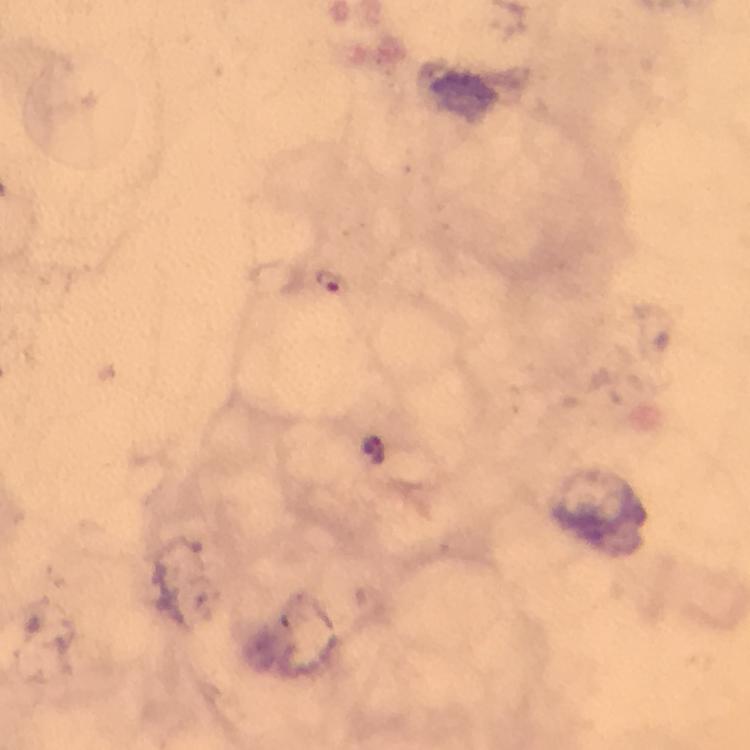

stain = Giemsa
preparation = thick blood film
cropped from = a single field of view
capture = smartphone camera through the microscope
immersion oil = applied
image size = 750×750 pixels
magnification = 100x
Plasmodium parasite locations = approximate centers as [x, y] in pixels: [330, 280]
context = from a malaria diagnostic workup